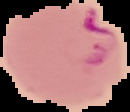
Result: Plasmodium parasites detected. From a thin blood smear. The area outside the segmented cell region is set to black. Image is 130×112 pixels.